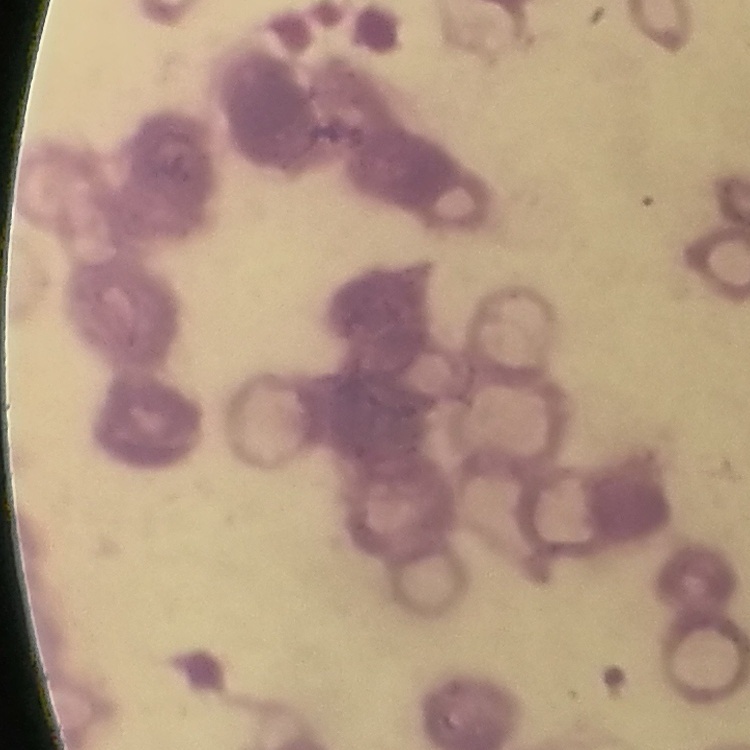
erythrocyte morphology = rouleaux formation
image type = one tile cut from a larger photomicrograph
stain = Field's or Giemsa
preparation = thin blood smear